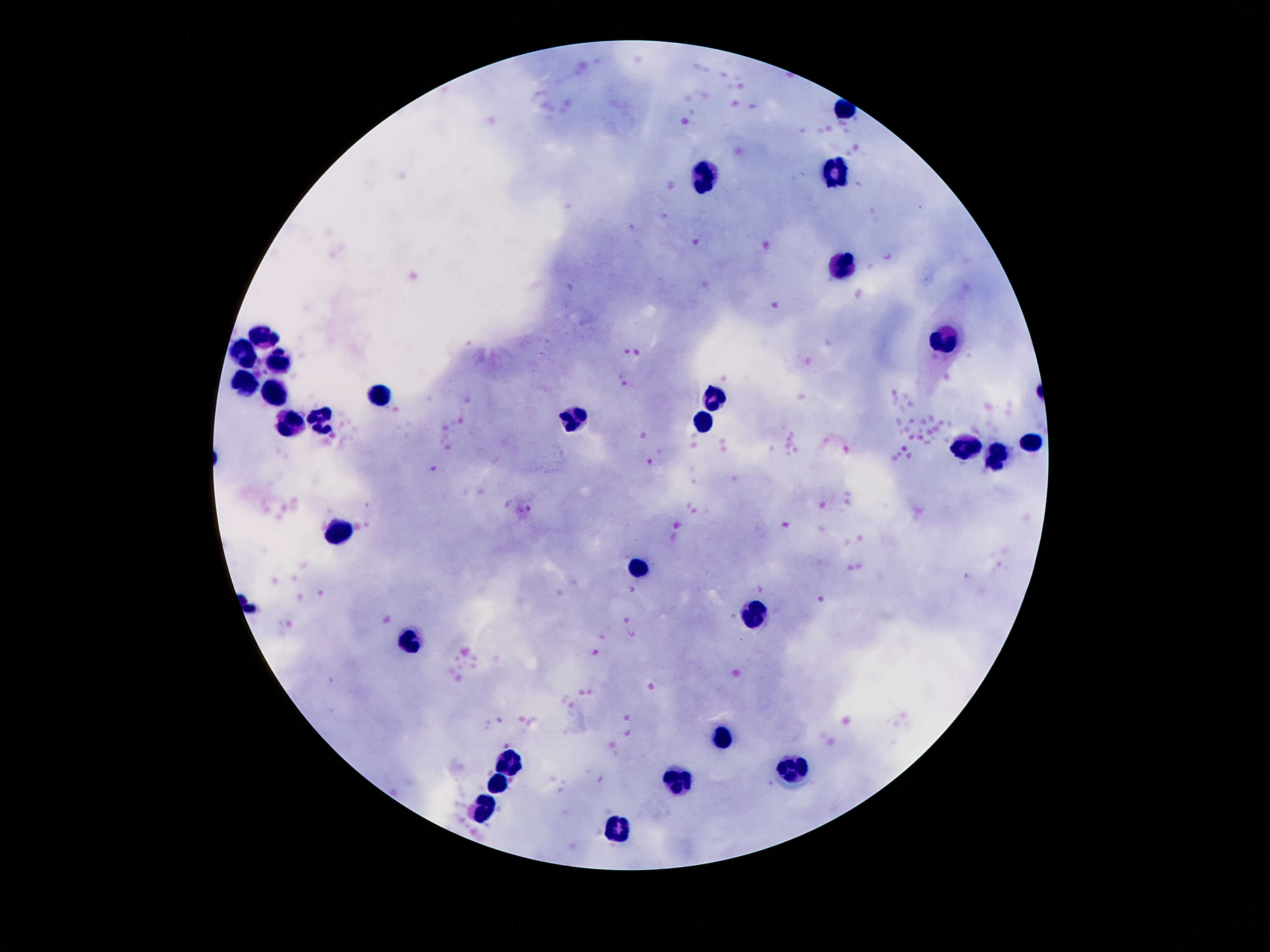 Approximate object centers, in pixels from the top-left corner. Leukocyte locations: (x=835, y=175), (x=707, y=178), (x=837, y=265), (x=264, y=337), (x=944, y=340), (x=245, y=354), (x=279, y=365), (x=245, y=382), (x=274, y=395), (x=379, y=395), (x=713, y=395), (x=575, y=421), (x=321, y=422), (x=701, y=422), (x=289, y=425), (x=1032, y=441), (x=969, y=447), (x=996, y=456), (x=341, y=529), (x=640, y=571), (x=755, y=613), (x=409, y=639), (x=721, y=738), (x=509, y=765), (x=789, y=772), (x=682, y=777), (x=497, y=786), (x=484, y=813), (x=619, y=830). Photographed through the microscope eyepiece with a smartphone camera. 100x magnification. Patient malaria status: not infected. Image is 1270×952 pixels. Giemsa-stained preparation. One field from this slide. Thick blood film.